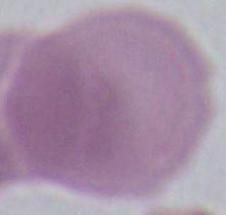

modality = photomicrograph
identification = red blood cell
magnification = 1000x